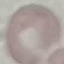
Malaria status: uninfected. Photographed with a smartphone camera at the microscope eyepiece. Thin blood smear. Giemsa-stained preparation. Cell patch, automatically extracted from a larger field of view and resized to 64 × 64 pixels.